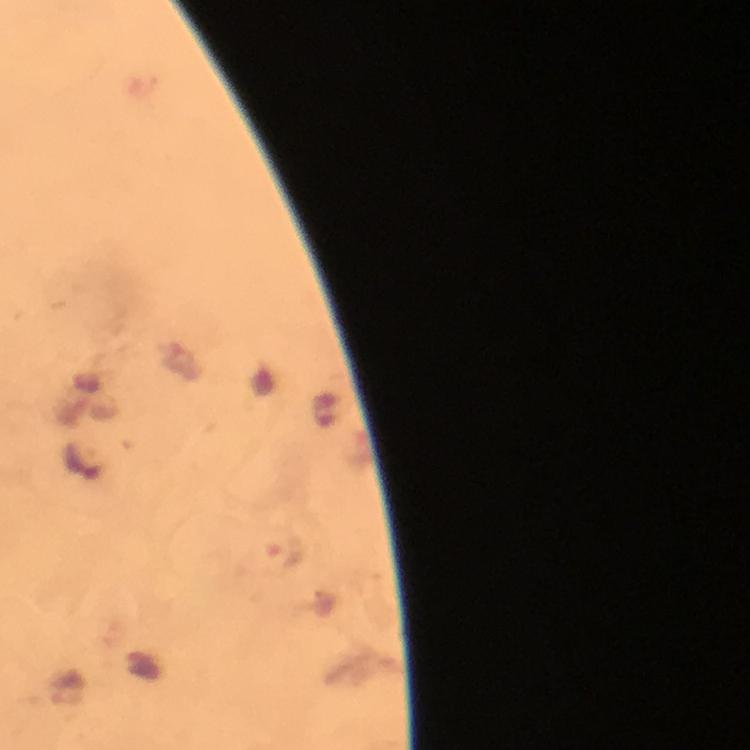 Approximate centers as (x, y) in pixels. Plasmodium parasite locations: (286, 552). Giemsa-stained preparation. Photographed with a smartphone mounted on the microscope. 100x magnification. From a malaria diagnostic workup. Thick blood smear. A crop from one field of view. Image is 750×750 pixels. Immersion oil applied.